Classify this cell by malaria status.
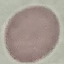

It is uninfected.

Giemsa-stained preparation. Photographed with a smartphone camera at the microscope eyepiece. Thin smear of blood. Cell patch, automatically extracted from a larger field of view and resized to 64 × 64 pixels.